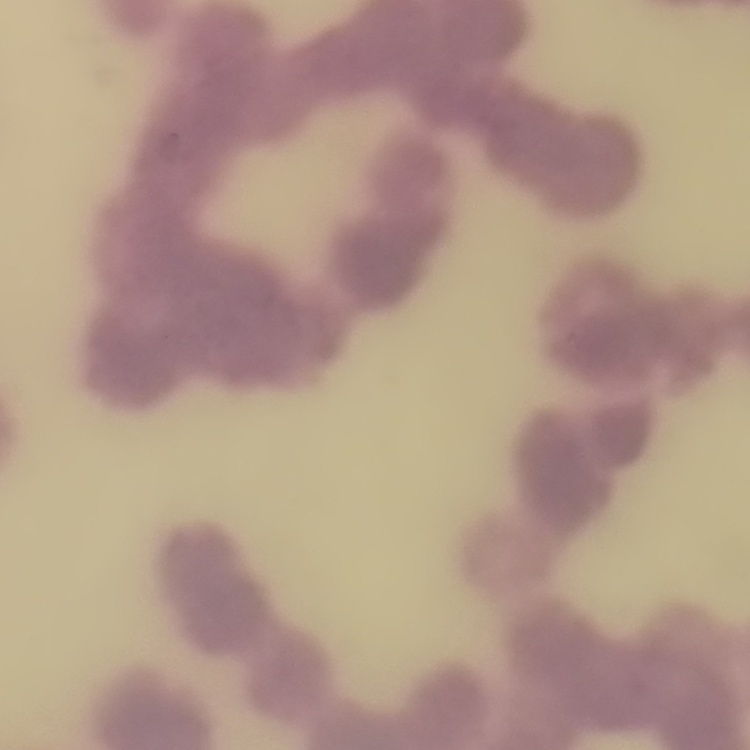
The erythrocytes show rouleaux formation. One tile cut from a larger photomicrograph. Field's or Giemsa stain. Thin peripheral smear.